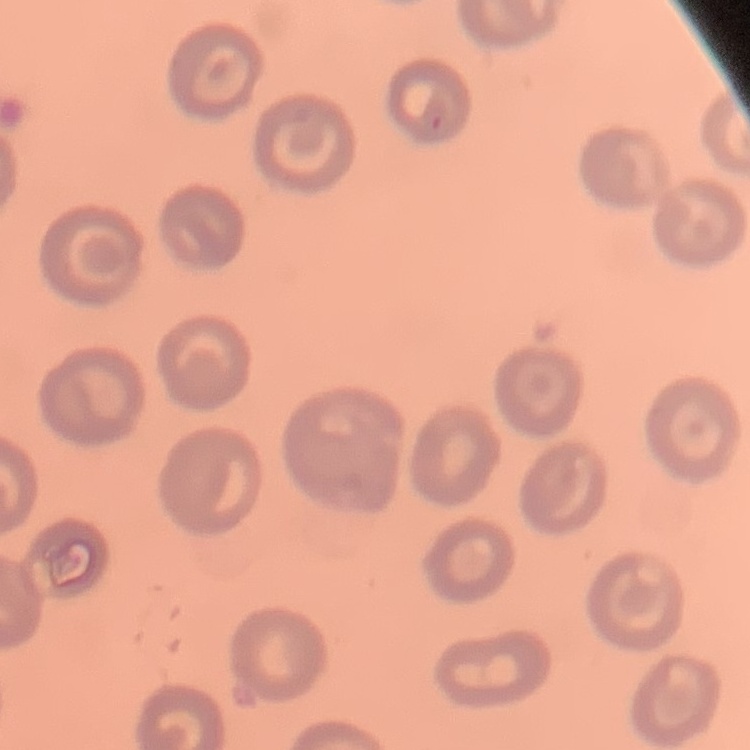

{
  "red_blood_cell_morphology": "no rouleaux formation",
  "preparation": "thin peripheral smear",
  "image_type": "one tile cut from a larger photomicrograph",
  "stain": "Field's or Giemsa"
}